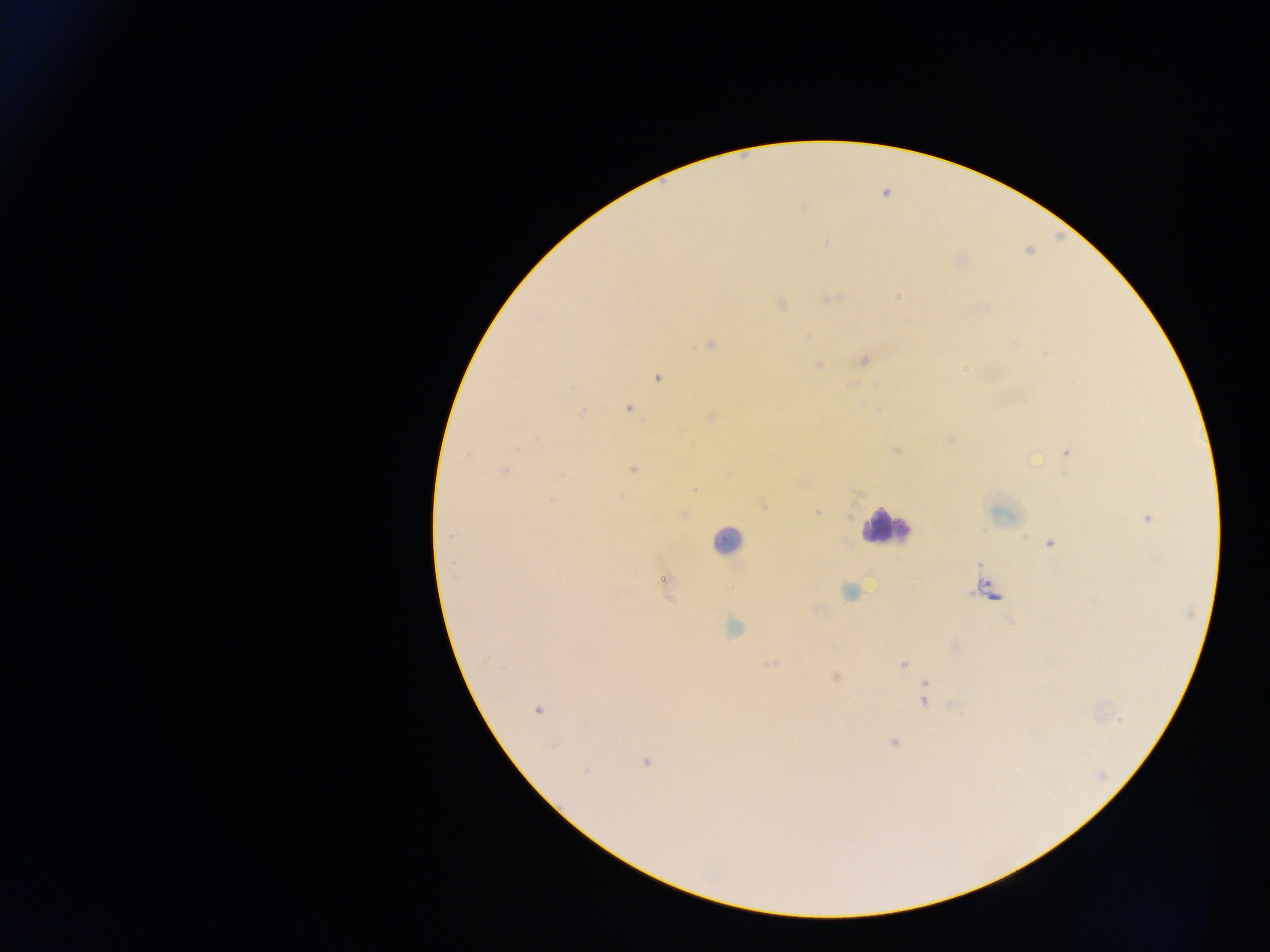 Approximate centers as (x, y) in pixels. Malaria parasite locations: (781, 305), (710, 345), (864, 360), (819, 365), (658, 378), (628, 409), (583, 412), (711, 417), (896, 451), (1067, 452), (467, 453), (1034, 461), (505, 469), (633, 469), (695, 491), (762, 505), (817, 512), (1147, 518), (449, 537), (1050, 544), (662, 579), (989, 591), (849, 592), (733, 628), (771, 665), (903, 665), (836, 676), (925, 699), (536, 710), (893, 742), (646, 763), (586, 770). Leukocyte locations: (886, 526), (726, 540). One field of view. Thick blood smear. Mobile-phone photograph taken through the microscope. Image is 1270×952 pixels. Collected in Ghana.